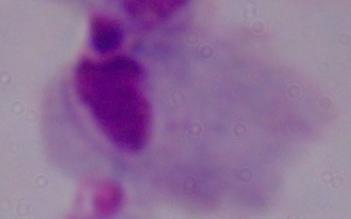

{
  "modality": "micrograph",
  "magnification": "1000x",
  "identification": "trichomonad"
}